Identify the parasite.
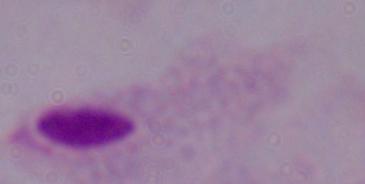

This is a trichomonad.

Captured at 1000x magnification. Photomicrograph.